Identify the parasite.
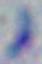
Toxoplasma gondii.

modality = micrograph
magnification = 1000x